State which parasite is depicted.
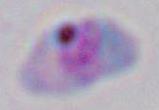

This is Toxoplasma gondii.

magnification: 1000x
modality: photomicrograph